Report the malaria status of this cell.
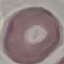

Uninfected.

Summary:
  - Preparation: thin blood smear
  - Image type: cell patch, automatically extracted from a larger field of view and resized to 64 × 64 pixels
  - Stain: Giemsa
  - Capture: smartphone through the microscope eyepiece